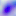

identification = Toxoplasma gondii
magnification = 400x
modality = photomicrograph